Locate every Plasmodium falciparum-infected red blood cell.
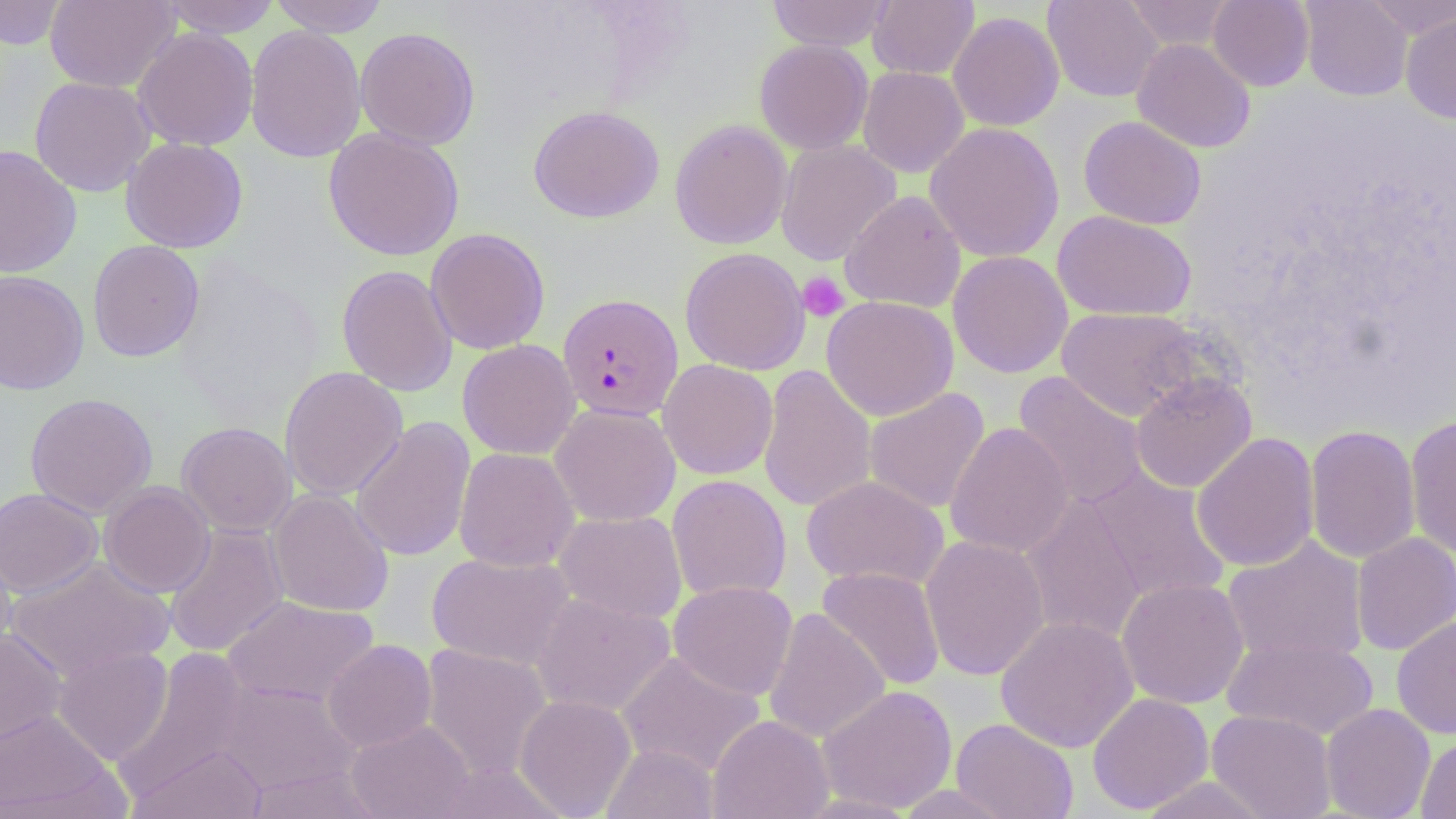
Approximate bounding boxes as (x1,y1)-(x2,y2) corner pairs in pixels.
Plasmodium falciparum-infected red blood cells: (557,293)-(683,422).

Uninfected red blood cell locations: (0,0)-(68,50), (44,0)-(179,93), (156,0)-(283,37), (268,0)-(390,36), (766,0)-(894,52), (868,0)-(979,79), (1043,0)-(1163,103), (1123,0)-(1236,51), (1208,0)-(1314,91), (1299,0)-(1413,101), (1364,0)-(1456,41), (948,11)-(1064,131), (1401,12)-(1456,124), (245,24)-(367,164), (133,27)-(258,151), (355,27)-(480,150), (1132,38)-(1255,153), (755,39)-(873,154), (858,66)-(969,177), (29,77)-(156,197), (528,105)-(664,223), (1078,116)-(1207,230), (670,119)-(793,250), (924,122)-(1064,263), (323,127)-(464,261), (121,137)-(248,253), (775,140)-(901,266), (0,145)-(83,279), (840,190)-(966,313), (1052,210)-(1197,321), (425,227)-(550,354), (87,239)-(205,362), (679,247)-(810,375), (948,251)-(1073,378), (337,264)-(458,397), (0,269)-(90,395), (821,295)-(958,420), (1056,307)-(1207,422), (1082,334)-(1232,467), (457,339)-(580,459), (658,359)-(778,480), (757,364)-(876,514), (279,366)-(408,501), (1012,371)-(1149,511), (1130,372)-(1257,493), (864,387)-(990,514), (24,392)-(158,518), (550,403)-(681,527), (1405,415)-(1456,559), (350,416)-(476,562), (177,421)-(297,536), (945,422)-(1073,558), (1304,424)-(1420,564), (1191,432)-(1320,572), (454,447)-(579,572), (1086,469)-(1230,605), (667,474)-(792,603), (801,475)-(950,591), (99,482)-(215,597), (0,487)-(103,597), (267,488)-(394,617), (1021,492)-(1151,646), (553,510)-(688,624), (163,523)-(290,658), (1351,532)-(1456,655), (920,534)-(1050,681), (1222,536)-(1369,666), (0,538)-(17,661), (426,551)-(576,671), (7,556)-(175,681), (816,566)-(946,691), (1116,576)-(1250,709), (668,580)-(798,701), (531,593)-(676,717), (222,595)-(380,709), (763,608)-(889,745), (1391,614)-(1456,739), (995,616)-(1139,753), (0,628)-(67,747), (1222,636)-(1379,741), (322,639)-(437,753), (420,643)-(554,781), (52,645)-(174,765), (616,652)-(766,778), (215,680)-(360,796), (817,685)-(957,813), (1087,692)-(1214,814), (514,694)-(637,817), (1321,703)-(1435,819), (1207,709)-(1337,819), (0,710)-(117,817), (707,715)-(834,818), (951,718)-(1079,819), (346,719)-(476,819), (1416,735)-(1456,819), (130,743)-(268,818), (600,743)-(721,819), (244,765)-(382,818), (1135,776)-(1275,818), (894,784)-(1017,818). Platelet locations: (797,271)-(850,322). Slide-level diagnosis: Plasmodium falciparum. Thin blood smear. Light microscopy. Image is 1456×819 pixels. 1000x magnification. Single field of view. May-Grünwald-Giemsa-stained preparation.